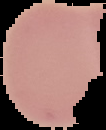
Result: no malaria parasites detected. From a thin blood film. Image is 106×130 pixels. The area outside the segmented cell region is set to black.